Identify the parasite.
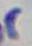

This is Toxoplasma gondii.

Summary:
  - Magnification: 1000x
  - Modality: photomicrograph